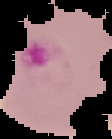 Result: malaria parasites identified. The area outside the segmented cell region is set to black. Image is 112×139 pixels. From a thin blood film.